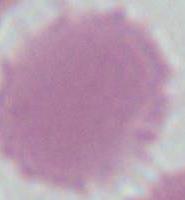
Micrograph. Captured at 1000x magnification. An erythrocyte is seen.